Outline each blood parasite and name the species.
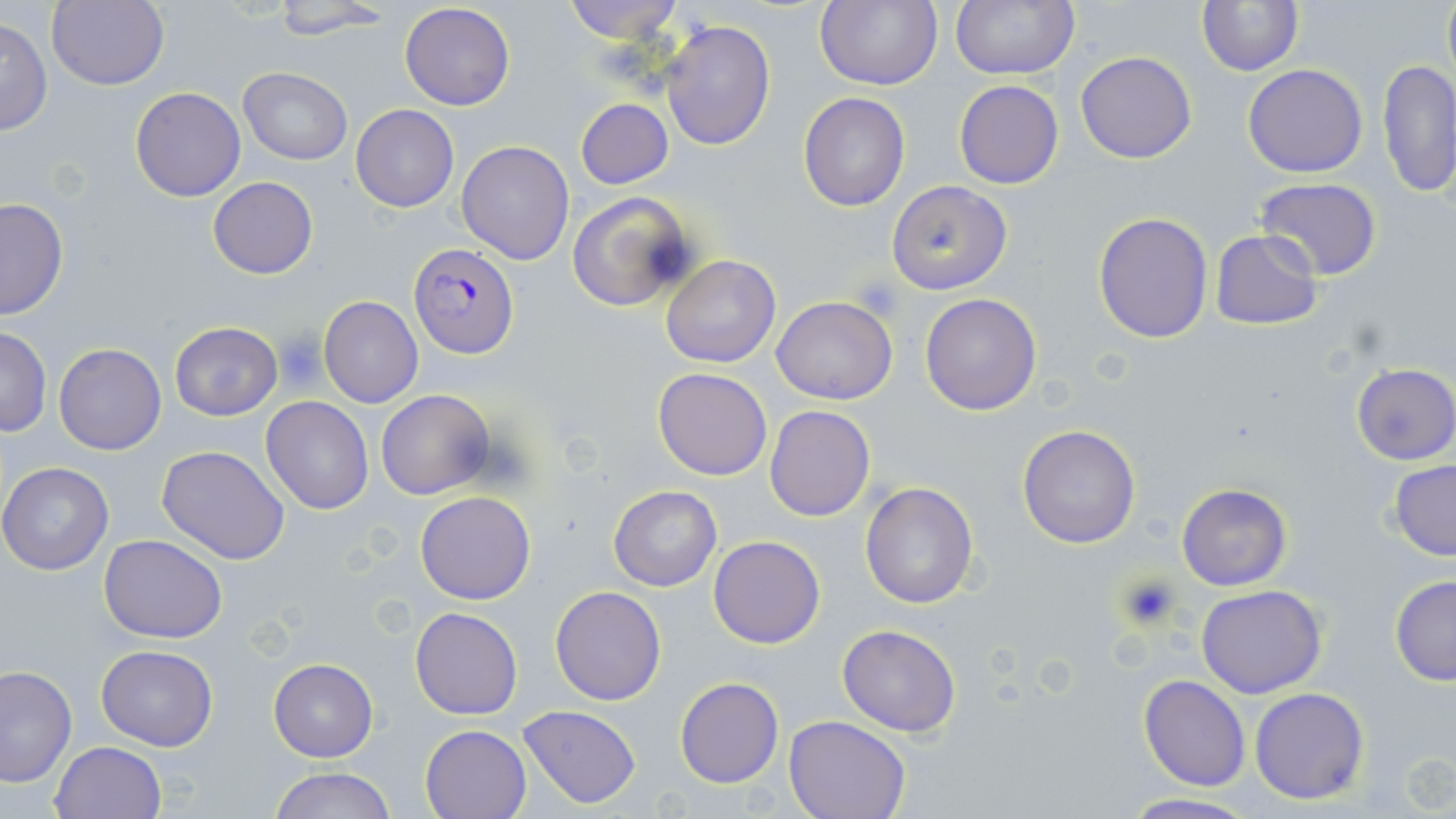

Approximate bounding boxes as [x1, y1, x2, y2] in pixels.
Plasmodium falciparum-infected red blood cells: [408, 243, 519, 358].
No Plasmodium ovale, Plasmodium malariae, Plasmodium vivax, Babesia divergens, or Trypanosoma brucei observed.

{
  "slide_level_diagnosis": "Plasmodium falciparum",
  "platelet_locations": "approximate bounding boxes as [x1, y1, x2, y2] in pixels: [855, 275, 903, 318], [274, 332, 328, 388], [1115, 572, 1182, 630]",
  "stain": "May-Grünwald-Giemsa",
  "uninfected_red_blood_cell_locations": "approximate bounding boxes as [x1, y1, x2, y2] in pixels: [560, 0, 684, 44], [814, 0, 942, 90], [950, 0, 1077, 80], [1441, 0, 1456, 88], [47, 1, 167, 89], [265, 1, 392, 40], [1196, 2, 1302, 75], [399, 3, 516, 112], [1, 15, 52, 138], [660, 19, 775, 152], [1075, 50, 1198, 164], [1377, 57, 1455, 198], [1243, 64, 1368, 178], [239, 68, 352, 164], [953, 80, 1064, 190], [130, 87, 245, 202], [798, 93, 910, 211], [576, 98, 673, 189], [351, 105, 458, 212], [457, 139, 575, 266], [207, 177, 318, 280], [1253, 177, 1383, 280], [886, 180, 1012, 295], [567, 191, 697, 311], [0, 197, 69, 320], [1092, 212, 1214, 343], [1210, 230, 1324, 330], [660, 254, 781, 370], [919, 293, 1041, 416], [319, 296, 422, 407], [771, 296, 897, 405], [170, 323, 282, 419], [0, 327, 50, 437], [54, 343, 166, 455], [1351, 362, 1456, 466], [653, 367, 772, 480], [375, 390, 496, 498], [261, 397, 375, 514], [765, 404, 876, 522], [1016, 424, 1142, 550], [157, 444, 291, 565], [1388, 460, 1456, 560], [0, 462, 114, 575], [859, 482, 979, 608], [1176, 482, 1291, 590], [609, 485, 721, 591], [415, 492, 535, 605], [99, 534, 227, 643], [708, 535, 825, 648], [1389, 575, 1456, 686], [1196, 584, 1327, 699], [550, 586, 667, 705], [410, 606, 523, 720], [836, 624, 961, 736], [95, 644, 218, 750], [268, 659, 378, 763], [0, 665, 76, 788], [1138, 673, 1251, 790], [675, 678, 784, 787], [1249, 687, 1370, 805], [518, 705, 642, 809], [785, 714, 910, 818], [421, 724, 532, 818], [49, 740, 166, 819], [268, 766, 397, 819], [1116, 792, 1263, 819]",
  "image_size": "1456×819 pixels",
  "magnification": "1000x",
  "field_of_view": "single",
  "modality": "light microscopy",
  "preparation": "thin blood smear"
}